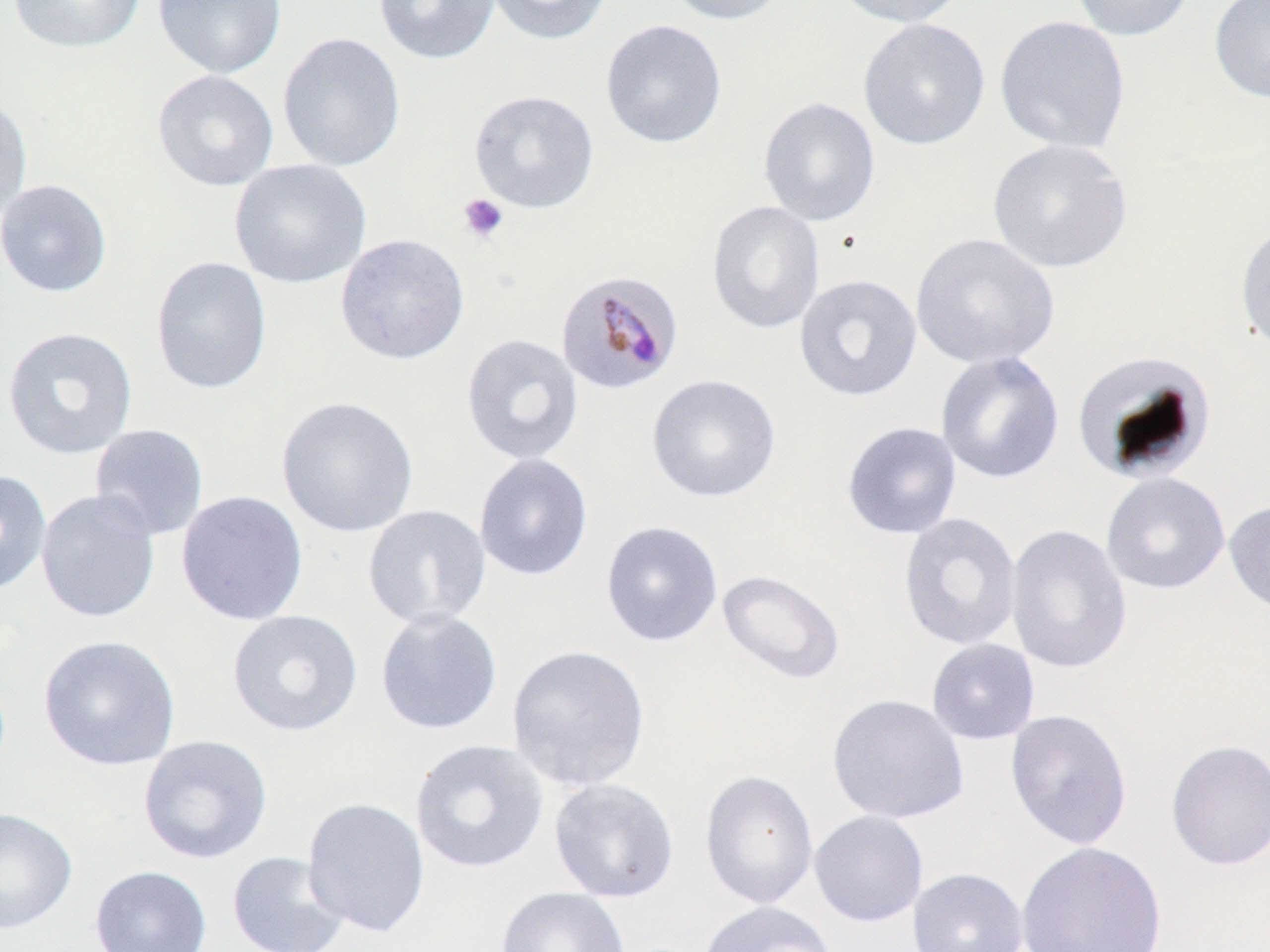
Summary:
  - Coordinate format: approximate bounding boxes as (x1,y1)-(x2,y2) corner pairs in pixels
  - Platelet locations: (457,193)-(509,244)
  - Plasmodium malariae-infected red blood cell locations: (554,267)-(685,395)
  - Uninfected red blood cell locations: (7,0)-(145,54), (153,0)-(287,79), (373,0)-(501,65), (483,0)-(613,46), (659,0)-(792,26), (831,0)-(969,29), (1069,0)-(1198,42), (1209,0)-(1270,104), (994,15)-(1131,155), (858,18)-(991,151), (600,19)-(727,149), (277,32)-(406,173), (152,70)-(279,191), (469,89)-(600,214), (0,95)-(33,227), (757,96)-(881,226), (987,138)-(1133,274), (229,159)-(372,289), (0,179)-(113,297), (706,200)-(825,335), (1234,220)-(1270,357), (910,232)-(1059,369), (335,233)-(470,365), (150,255)-(272,396), (794,273)-(923,402), (2,326)-(139,460), (461,332)-(584,465), (1071,348)-(1216,484), (936,350)-(1065,485), (646,373)-(781,503), (276,395)-(419,538), (841,421)-(962,539), (88,424)-(210,541), (473,453)-(593,581), (0,469)-(52,595), (1101,472)-(1230,595), (36,490)-(162,624), (175,490)-(309,626), (1224,499)-(1270,618), (362,504)-(491,629), (898,512)-(1022,651), (600,520)-(724,648), (1005,524)-(1132,674), (716,568)-(846,685), (375,608)-(503,735), (227,609)-(363,737), (38,635)-(180,771), (926,638)-(1040,745), (506,644)-(651,792), (827,693)-(969,824), (1005,709)-(1132,850), (138,734)-(273,864), (410,738)-(549,873), (1165,739)-(1270,871), (699,769)-(819,909), (548,777)-(680,903), (302,796)-(430,938), (0,807)-(78,934), (809,810)-(929,927), (1015,841)-(1168,952), (226,850)-(352,952), (89,865)-(212,952), (907,867)-(1029,952), (496,886)-(630,952), (696,900)-(838,952)
  - Slide-level diagnosis: Plasmodium malariae
  - Image size: 1270×952 pixels
  - Stain: May-Grünwald-Giemsa
  - Preparation: thin blood smear
  - Modality: optical microscopy
  - Field of view: single
  - Magnification: 1000x